Draw a bounding box around every parasitised red blood cell.
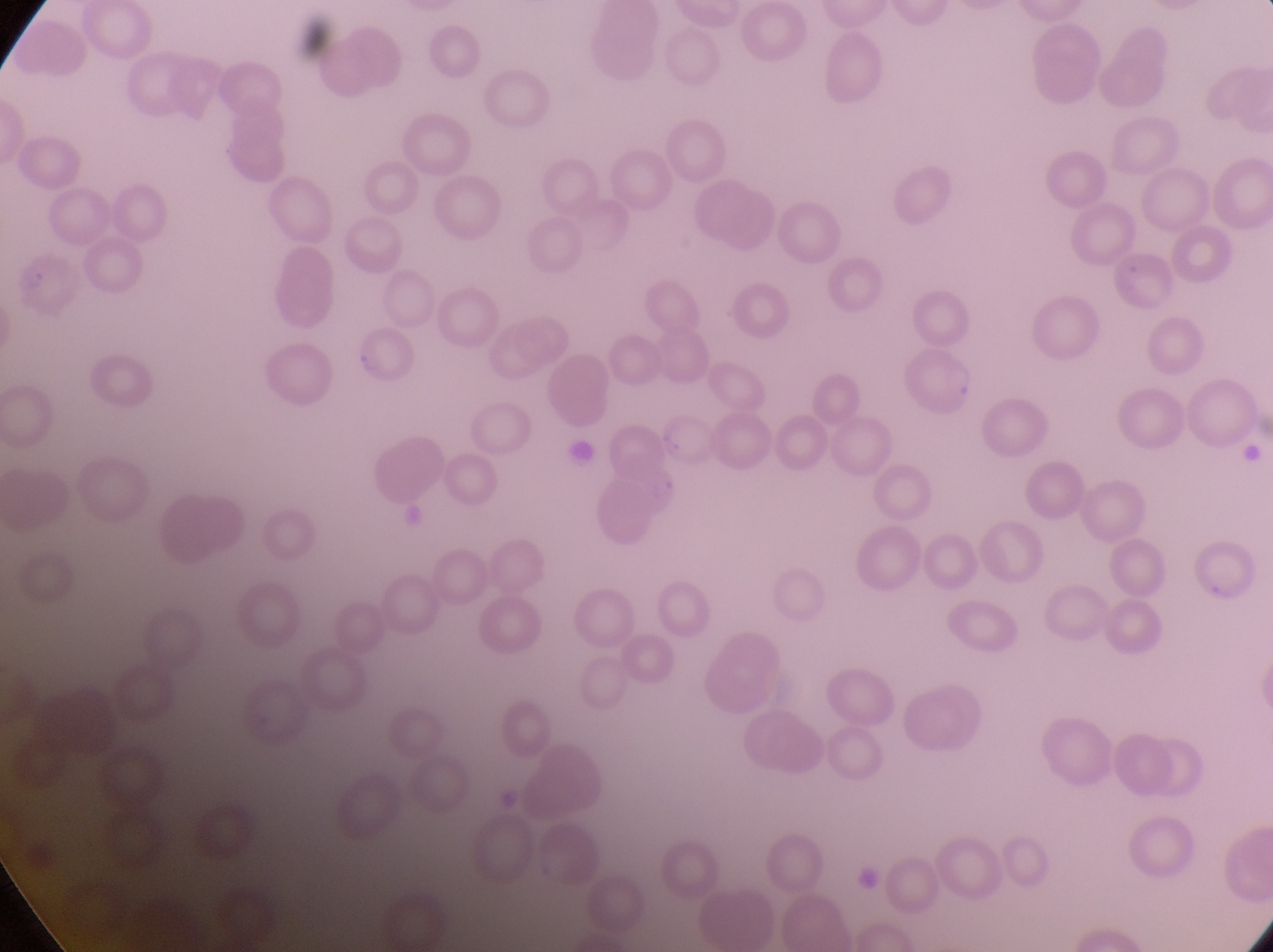

Approximate bounding boxes as {left, top, right, bottom} in pixels.
Parasitised red blood cells: {12, 250, 92, 328}, {354, 329, 423, 394}, {908, 344, 983, 416}.

Artifact (platelet-like body, stain precipitate, or debris) locations: {561, 432, 603, 471}. Thin blood film. At a magnification of 1000x. Image is 1273×952 pixels. Photographed through the eyepiece of an Olympus CX-23 microscope with a smartphone camera. Single field of view. Sample from Uganda.